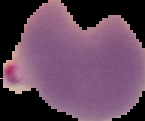 From a thin blood smear. The area outside the segmented cell region is set to black. Image is 145×121 pixels. Malaria status: parasitized.